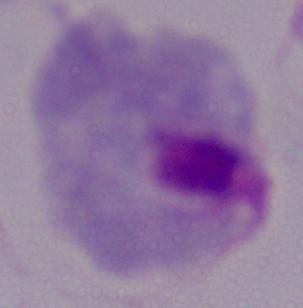

modality = photomicrograph
identification = trichomonad
magnification = 1000x